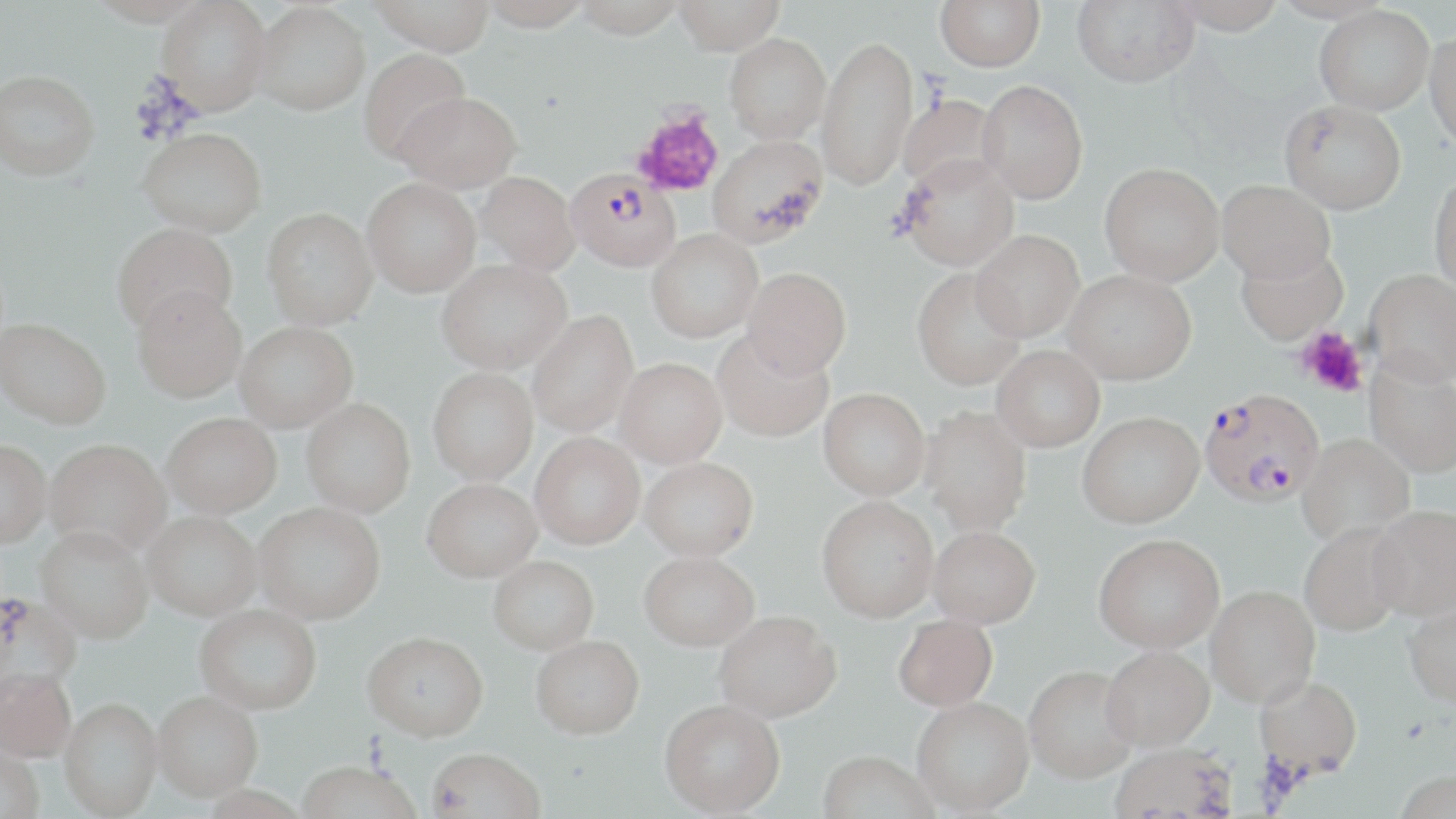 Approximate bounding boxes as (x1,y1)-(x2,y2) corner pairs in pixels. Platelet locations: (632,108)-(725,198), (1295,325)-(1368,397). Uninfected red blood cell locations: (86,0)-(208,26), (156,0)-(272,115), (371,0)-(494,55), (481,0)-(591,32), (574,0)-(685,38), (673,0)-(785,55), (936,0)-(1045,71), (1071,0)-(1199,88), (250,2)-(370,115), (1314,5)-(1434,114), (1424,30)-(1456,153), (724,33)-(830,144), (816,35)-(918,190), (359,48)-(471,163), (0,69)-(99,180), (977,80)-(1087,204), (396,92)-(521,192), (897,94)-(1004,193), (1280,99)-(1406,215), (138,127)-(266,236), (707,134)-(829,249), (898,154)-(1018,271), (1098,163)-(1224,286), (476,171)-(580,274), (1428,173)-(1456,297), (362,178)-(481,297), (1217,180)-(1335,288), (262,208)-(378,330), (112,222)-(238,334), (646,230)-(763,343), (970,231)-(1083,343), (1235,246)-(1348,347), (436,258)-(571,373), (743,266)-(851,379), (911,268)-(1026,390), (1063,272)-(1196,389), (1364,272)-(1456,393), (132,285)-(246,403), (526,311)-(639,437), (0,316)-(111,429), (234,321)-(358,431), (711,329)-(834,443), (992,347)-(1105,455), (615,357)-(727,467), (1364,361)-(1456,481), (428,367)-(538,485), (817,388)-(929,501), (301,398)-(415,517), (919,407)-(1032,538), (162,412)-(282,517), (1077,416)-(1205,533), (530,433)-(645,549), (1297,436)-(1415,548), (43,439)-(171,559), (0,442)-(50,551), (640,457)-(759,561), (422,478)-(542,582), (817,499)-(938,624), (254,503)-(386,626), (1368,510)-(1456,626), (142,511)-(261,622), (1300,526)-(1408,638), (928,529)-(1040,631), (35,530)-(154,646), (1094,539)-(1224,658), (639,551)-(759,650), (488,555)-(599,654), (1206,589)-(1321,712), (0,593)-(82,706), (1403,604)-(1456,715), (194,605)-(322,717), (714,611)-(841,723), (892,615)-(997,713), (363,633)-(489,743), (531,635)-(644,738), (1102,651)-(1215,756), (1024,670)-(1138,787), (0,673)-(76,766), (1254,679)-(1362,786), (152,695)-(263,805), (659,699)-(785,818), (912,699)-(1034,817), (59,702)-(163,819), (0,743)-(45,819), (1109,748)-(1236,819), (427,750)-(546,819), (816,753)-(939,819), (294,765)-(422,819), (1391,776)-(1456,818), (200,788)-(311,819). Plasmodium falciparum-infected red blood cell locations: (566,169)-(681,272), (1199,394)-(1324,511). Slide-level diagnosis: Plasmodium falciparum. Single field of view. May-Grünwald-Giemsa-stained preparation. Image is 1456×819 pixels. Thin blood film. Optical microscopy. Captured at 1000x magnification.